Point out each leukocyte.
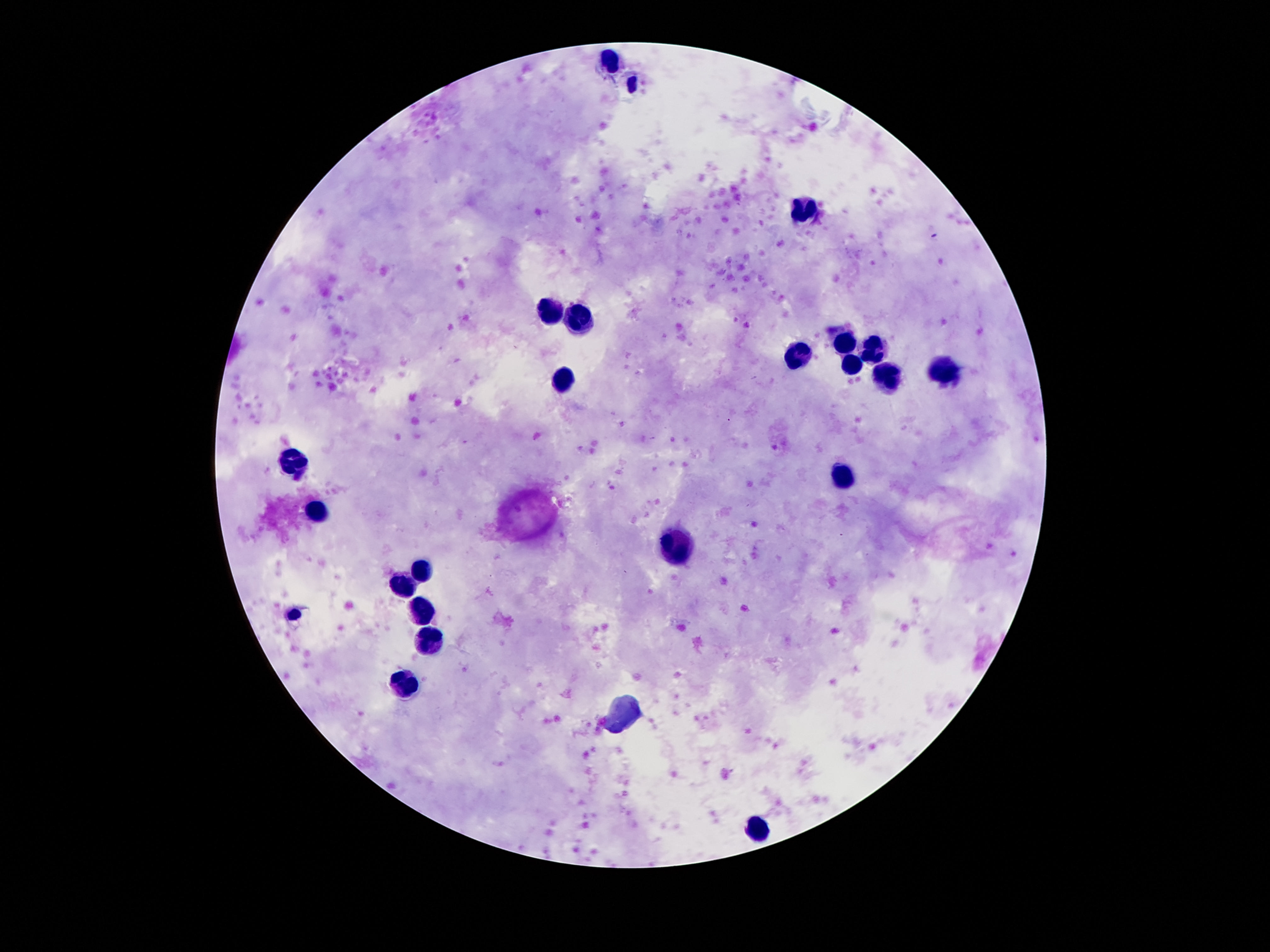

Approximate centers as (x, y) in pixels.
Leukocytes: (611, 60), (806, 209), (550, 310), (576, 318), (843, 343), (871, 351), (800, 353), (851, 367), (943, 372), (884, 377), (564, 378), (294, 463), (841, 476), (316, 513), (681, 546), (423, 568), (400, 588), (421, 611), (429, 640), (406, 683), (763, 826).

Patient malaria status: negative. Image is 1270×952 pixels. Smartphone photograph taken through the microscope eyepiece. Single field of view. Giemsa stain. 100x magnification. Thick blood smear.